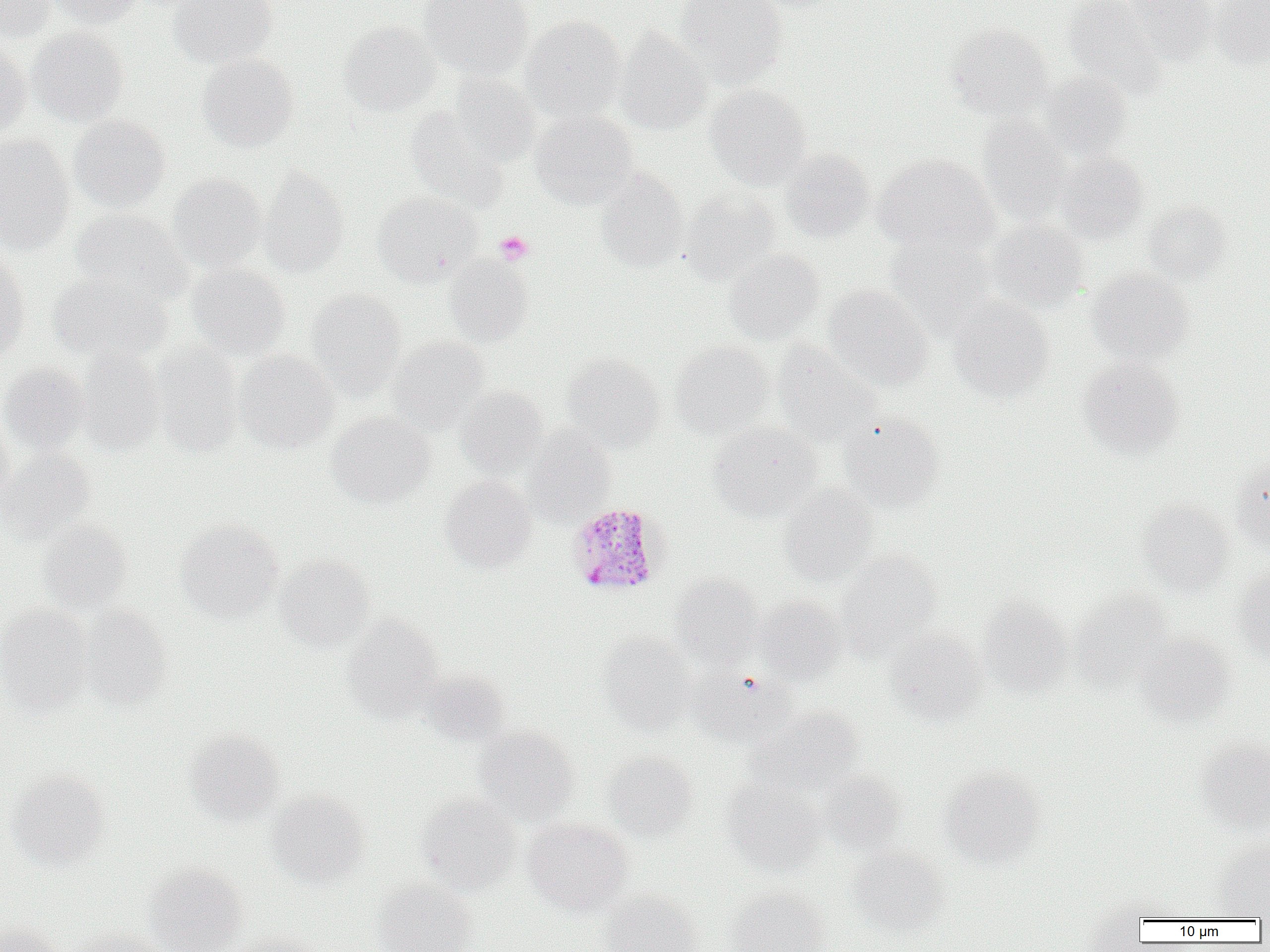

Approximate bounding boxes as (x1, y1, x2, y2) in pixels. Uninfected red blood cell locations: (0, 0, 56, 42), (47, 0, 144, 28), (169, 0, 277, 69), (419, 0, 533, 80), (674, 0, 787, 87), (1061, 0, 1166, 97), (1124, 0, 1219, 65), (1211, 0, 1270, 68), (520, 16, 627, 120), (339, 21, 441, 116), (947, 23, 1054, 120), (27, 27, 128, 126), (615, 28, 713, 135), (0, 39, 31, 136), (197, 54, 300, 152), (1039, 72, 1133, 160), (448, 73, 541, 167), (705, 85, 812, 191), (529, 108, 638, 209), (69, 115, 170, 211), (977, 117, 1071, 225), (0, 135, 75, 254), (779, 149, 874, 242), (1055, 152, 1148, 243), (874, 154, 1000, 259), (258, 165, 348, 278), (596, 169, 688, 272), (167, 174, 267, 272), (679, 189, 780, 284), (372, 191, 483, 286), (1143, 201, 1233, 285), (70, 208, 193, 305), (985, 220, 1090, 311), (884, 235, 1000, 338), (725, 249, 824, 344), (0, 252, 31, 360), (443, 255, 534, 346), (186, 262, 290, 360), (1087, 268, 1193, 363), (48, 271, 172, 365), (823, 285, 932, 390), (305, 289, 406, 398), (948, 296, 1054, 401), (387, 336, 489, 433), (669, 341, 772, 440), (772, 342, 882, 447), (151, 343, 244, 457), (76, 348, 164, 456), (235, 349, 338, 452), (561, 354, 664, 450), (1077, 357, 1184, 456), (0, 363, 90, 456), (455, 386, 548, 477), (328, 412, 434, 507), (839, 414, 945, 512), (0, 415, 15, 512), (708, 421, 821, 521), (525, 427, 616, 524), (1, 449, 95, 539), (1231, 456, 1270, 552), (440, 475, 536, 572), (780, 484, 878, 585), (1138, 498, 1234, 595), (38, 520, 132, 614), (176, 520, 284, 622), (836, 550, 941, 656), (276, 555, 375, 652), (1233, 566, 1270, 660), (669, 575, 763, 669), (1070, 589, 1175, 691), (755, 595, 846, 684), (978, 597, 1074, 698), (0, 604, 91, 714), (79, 606, 173, 710), (342, 614, 443, 721), (885, 629, 988, 725), (600, 633, 698, 735), (1135, 633, 1236, 726), (692, 669, 796, 746), (421, 670, 511, 747), (751, 707, 864, 796), (474, 726, 579, 824), (184, 728, 286, 825), (1195, 737, 1270, 834), (602, 750, 698, 841), (940, 767, 1045, 868), (6, 771, 109, 870), (816, 771, 903, 854), (723, 779, 828, 875), (267, 791, 370, 888), (416, 793, 520, 896), (523, 817, 633, 916), (1213, 837, 1270, 918), (849, 847, 949, 936), (144, 862, 248, 952), (373, 879, 477, 952), (725, 886, 830, 952), (601, 890, 703, 952), (0, 922, 63, 952), (70, 926, 169, 952), (228, 930, 322, 952). Platelet locations: (495, 231, 534, 265). Plasmodium malariae-infected red blood cell locations: (567, 502, 669, 598). Slide-level diagnosis: Plasmodium malariae. Thin blood film. 1000x magnification. Single field of view. Light microscopy. Image is 1270×952 pixels.